Assess this cell for malaria.
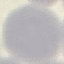
It is uninfected.

preparation: thin blood film
capture: smartphone through the microscope eyepiece
stain: Giemsa
image_type: automatically extracted cell patch, resized to 64 × 64 pixels